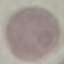
Summary:
  - Malaria status: uninfected
  - Image type: automatically extracted cell patch, resized to 64 × 64 pixels
  - Preparation: thin blood smear
  - Capture: smartphone camera at the microscope eyepiece
  - Stain: Giemsa